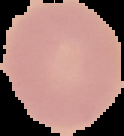

Summary:
  - Image type: segmented cell region with the area outside set to black
  - Preparation: thin blood film
  - Result: no malaria parasites detected
  - Image size: 124×136 pixels